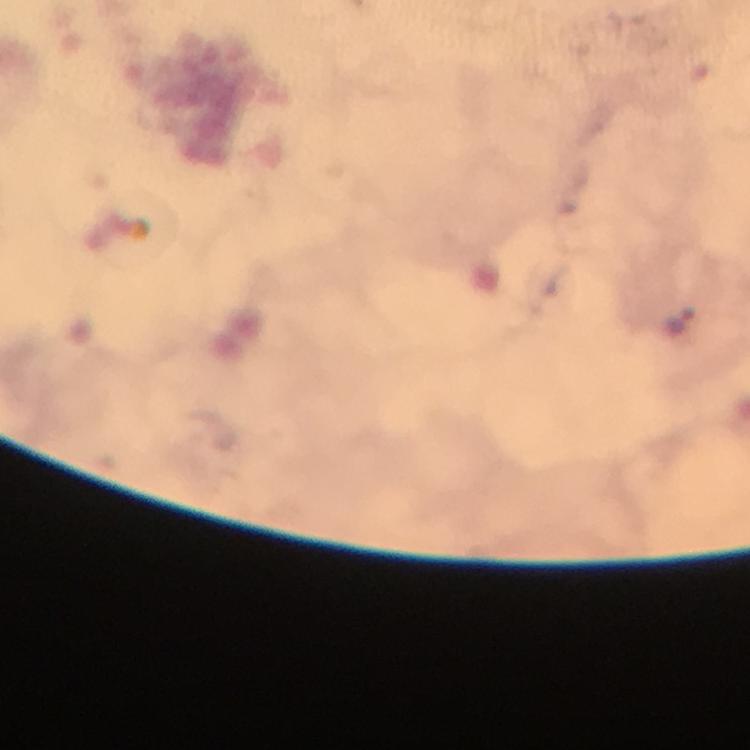
Approximate object centers, in pixels from the top-left corner. Malaria parasite locations: (x=681, y=320). A crop from one field of view. Photographed with a smartphone mounted on the microscope. 100x magnification. Giemsa-stained preparation. Thick blood smear. Image is 750×750 pixels. From a malaria diagnostic workup. Immersion oil was used.